Identify the parasite.
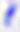

Toxoplasma gondii.

Photomicrograph. Captured at 400x magnification.